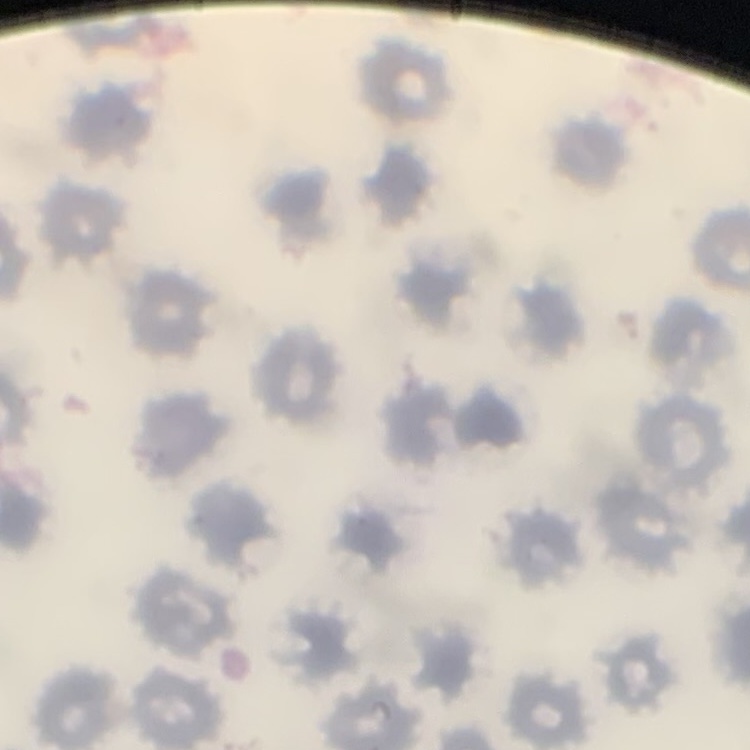

The red blood cells show no rouleaux formation. Square crop of a larger photomicrograph. Stained with either Field's or Giemsa. Thin blood smear.